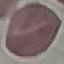 Malaria status: uninfected. Thin smear of blood. Acquired by smartphone through the microscope eyepiece. Cell patch, automatically extracted from a larger field of view and resized to 64 × 64 pixels. Giemsa stain.